Assess this cell for malaria.
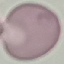
Uninfected.

image type = cell patch, automatically extracted from a larger field of view and resized to 64 × 64 pixels
stain = Giemsa
preparation = thin blood smear
capture = smartphone through the microscope eyepiece